Name the blood parasite species.
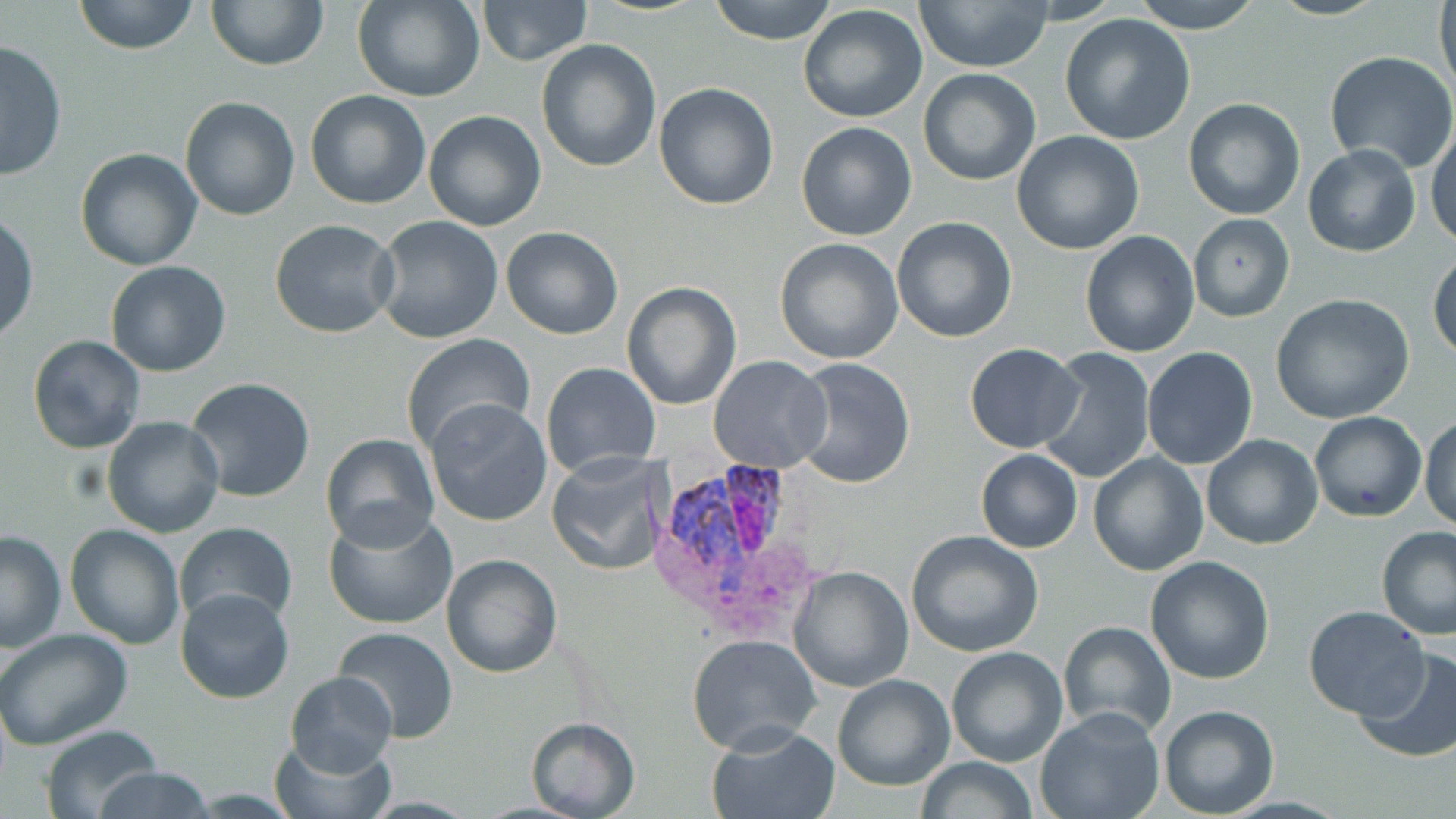

Plasmodium vivax.

Approximate bounding boxes as (x1, y1, x2, y2) in pixels. Uninfected red blood cell locations: (73, 0, 200, 55), (205, 0, 327, 71), (354, 0, 485, 102), (707, 0, 841, 45), (912, 0, 1056, 71), (1128, 0, 1266, 32), (1265, 0, 1386, 20), (1433, 0, 1455, 104), (477, 1, 591, 65), (798, 5, 930, 124), (1059, 12, 1196, 144), (0, 38, 67, 180), (536, 39, 662, 173), (1324, 50, 1456, 173), (917, 68, 1041, 186), (653, 82, 779, 211), (305, 90, 432, 210), (181, 96, 299, 221), (1183, 98, 1306, 221), (422, 109, 546, 230), (1426, 120, 1456, 250), (796, 121, 919, 241), (1011, 130, 1144, 255), (1302, 144, 1421, 257), (75, 147, 204, 270), (0, 211, 37, 343), (1188, 213, 1295, 322), (371, 216, 505, 344), (891, 217, 1017, 341), (269, 220, 401, 337), (501, 226, 623, 341), (1080, 230, 1199, 356), (773, 237, 903, 363), (1428, 248, 1456, 362), (104, 260, 232, 377), (621, 283, 740, 410), (1270, 293, 1416, 426), (400, 333, 535, 456), (26, 336, 147, 454), (965, 343, 1083, 452), (1140, 347, 1259, 469), (1035, 348, 1155, 485), (709, 355, 834, 473), (791, 357, 917, 489), (540, 362, 662, 479), (184, 377, 316, 503), (426, 400, 553, 526), (1309, 411, 1426, 522), (102, 415, 226, 538), (1420, 415, 1456, 531), (319, 433, 441, 552), (1201, 434, 1324, 550), (975, 449, 1082, 552), (547, 450, 668, 576), (1088, 451, 1210, 576), (322, 509, 459, 631), (175, 522, 298, 628), (63, 523, 186, 649), (1374, 525, 1456, 641), (0, 529, 68, 651), (905, 530, 1045, 659), (442, 554, 562, 677), (1146, 556, 1275, 684), (788, 565, 913, 692), (175, 588, 294, 705), (1303, 606, 1429, 719), (1058, 619, 1178, 739), (0, 628, 133, 749), (332, 628, 459, 745), (686, 633, 820, 752), (946, 646, 1067, 766), (1353, 647, 1456, 762), (284, 670, 397, 776), (833, 675, 954, 790), (1159, 704, 1279, 818), (1035, 707, 1165, 819), (525, 717, 641, 819), (708, 723, 842, 819), (38, 725, 164, 819), (271, 735, 392, 819), (912, 757, 1040, 817), (88, 767, 217, 819). Plasmodium vivax-infected red blood cell locations: (660, 455, 794, 591). Thin blood film. Single field of view. Image is 1456×819 pixels. May-Grünwald-Giemsa stain. Optical microscopy. 1000x magnification.